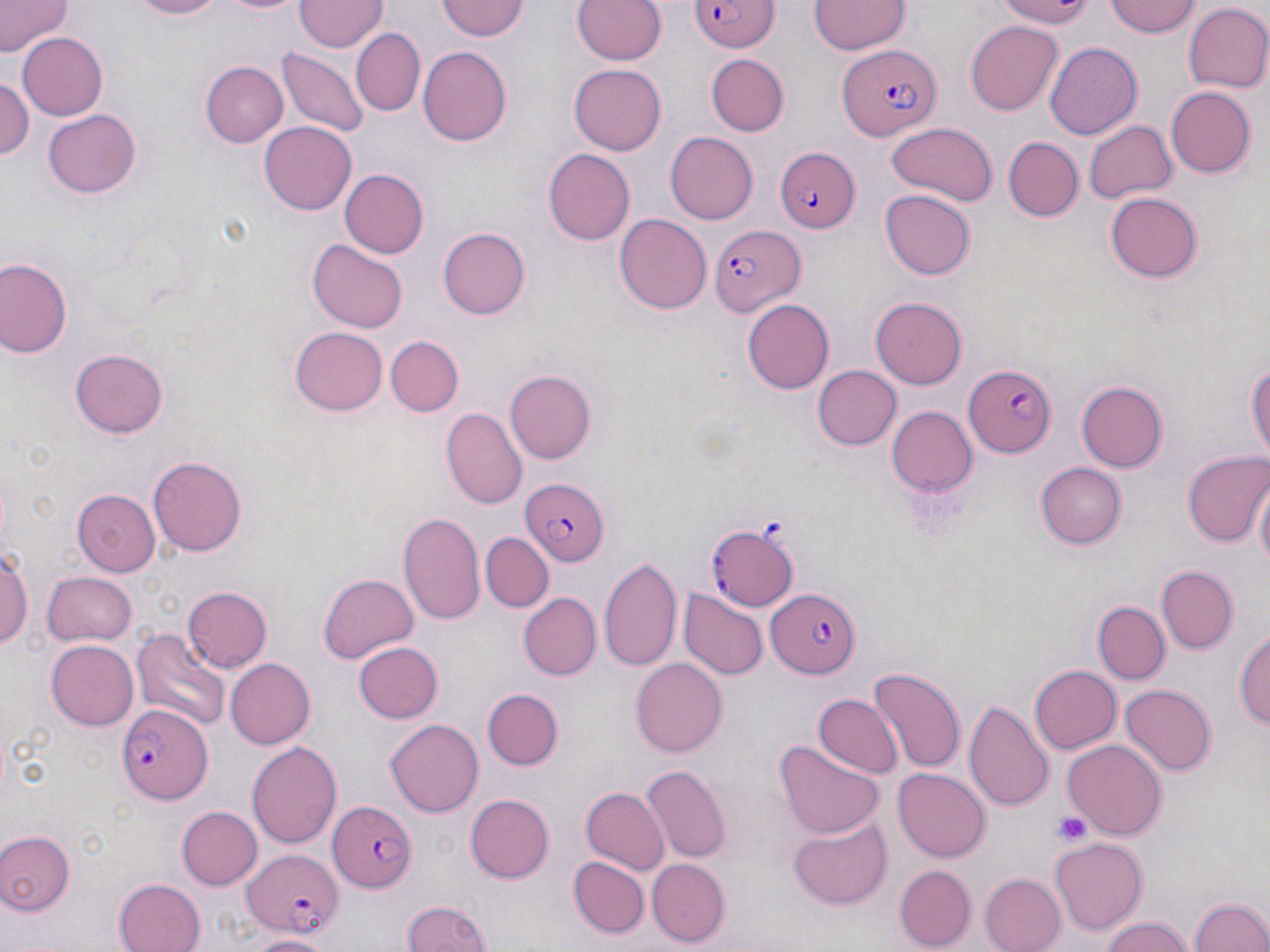

slide-level diagnosis = Plasmodium falciparum
image size = 1270×952 pixels
preparation = thin blood film
field of view = one of a larger specimen
magnification = 1000x
uninfected red blood cell locations = approximate bounding boxes as [x1, y1, x2, y2] in pixels: [0, 0, 69, 56], [128, 0, 233, 20], [218, 0, 308, 15], [296, 0, 387, 51], [573, 0, 666, 66], [993, 0, 1099, 27], [1104, 0, 1201, 39], [437, 1, 529, 42], [809, 2, 908, 56], [1184, 3, 1270, 93], [964, 19, 1063, 115], [349, 27, 425, 117], [18, 33, 107, 117], [1043, 42, 1141, 141], [280, 47, 368, 137], [418, 47, 513, 145], [707, 55, 789, 136], [201, 61, 289, 147], [569, 66, 666, 153], [0, 74, 33, 168], [1166, 86, 1256, 177], [43, 109, 142, 199], [1085, 120, 1178, 204], [260, 121, 356, 215], [886, 122, 997, 205], [664, 131, 758, 224], [1003, 136, 1083, 221], [546, 147, 636, 245], [340, 169, 429, 259], [880, 189, 976, 280], [1105, 191, 1201, 281], [614, 213, 712, 314], [438, 226, 530, 319], [306, 238, 409, 332], [0, 257, 74, 360], [870, 296, 968, 388], [741, 299, 833, 395], [290, 327, 387, 414], [386, 335, 463, 415], [70, 348, 168, 439], [1246, 352, 1270, 469], [811, 365, 900, 450], [505, 370, 597, 463], [1075, 381, 1166, 473], [885, 405, 977, 499], [442, 406, 527, 509], [1184, 452, 1270, 550], [148, 456, 248, 556], [1036, 462, 1126, 547], [1250, 473, 1269, 571], [72, 490, 161, 576], [398, 513, 485, 628], [481, 532, 553, 611], [1, 543, 33, 653], [599, 554, 684, 674], [1156, 566, 1239, 654], [41, 571, 135, 646], [319, 574, 418, 662], [182, 586, 272, 672], [680, 588, 766, 681], [519, 592, 601, 680], [1094, 601, 1169, 683], [1235, 622, 1270, 734], [133, 627, 229, 734], [45, 639, 139, 729], [353, 641, 442, 722], [225, 657, 314, 749], [630, 658, 726, 759], [1029, 665, 1122, 755], [867, 667, 966, 775], [1120, 683, 1215, 776], [480, 686, 564, 770], [813, 692, 901, 780], [965, 699, 1055, 815], [386, 719, 483, 817], [1064, 739, 1167, 841], [247, 740, 342, 847], [777, 743, 883, 837], [640, 765, 731, 863], [893, 767, 991, 862], [581, 786, 669, 874], [466, 794, 553, 882], [176, 806, 261, 889], [789, 814, 893, 909], [0, 830, 75, 914], [1051, 838, 1150, 931], [568, 857, 650, 937], [648, 858, 729, 946], [894, 867, 976, 949], [978, 874, 1066, 952], [113, 877, 205, 952], [1186, 894, 1270, 952], [400, 898, 497, 952], [1097, 915, 1196, 952], [248, 932, 336, 951]
stain = May-Grünwald-Giemsa
modality = optical microscopy
Plasmodium falciparum-infected red blood cell locations = approximate bounding boxes as [x1, y1, x2, y2] in pixels: [688, 0, 781, 50], [839, 47, 942, 140], [773, 148, 862, 231], [709, 220, 805, 316], [962, 363, 1055, 458], [519, 477, 608, 566], [710, 524, 798, 610], [768, 588, 863, 678], [119, 703, 212, 807], [328, 800, 416, 891], [241, 851, 345, 938]
platelet locations = approximate bounding boxes as [x1, y1, x2, y2] in pixels: [1051, 811, 1095, 848]